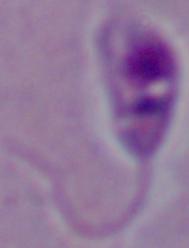
Summary:
  - Modality: micrograph
  - Identification: Leishmania
  - Magnification: 1000x